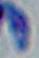

magnification = 1000x
modality = photomicrograph
identification = Toxoplasma gondii